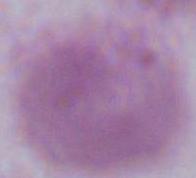
modality: photomicrograph
identification: erythrocyte
magnification: 1000x